Name the blood parasite species.
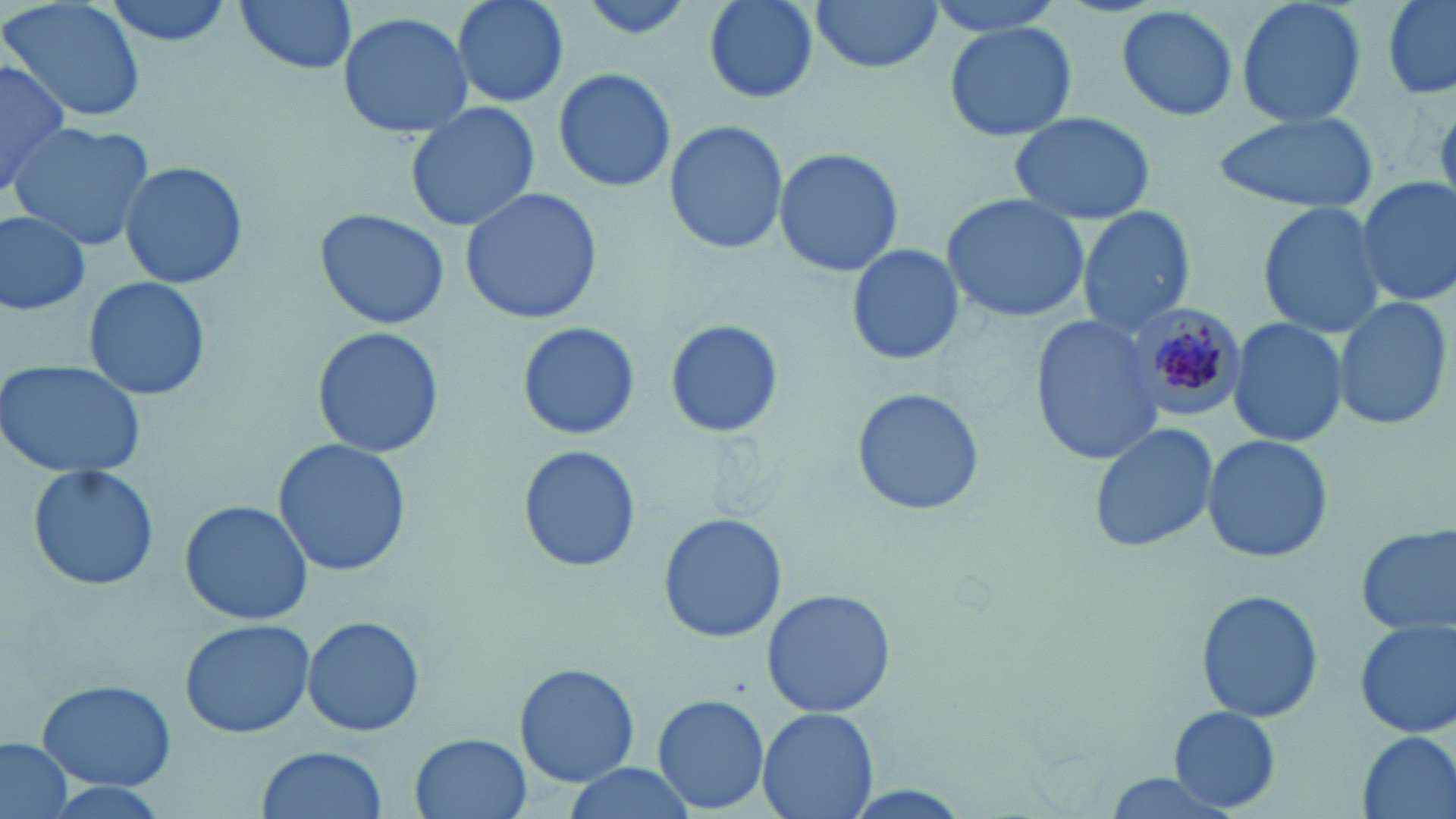

Plasmodium malariae.

Summary:
  - Coordinate format: approximate bounding boxes as named x1/y1/x2/y2 corners in pixels
  - Uninfected red blood cell locations: (x1=4, y1=0, x2=149, y2=123), (x1=101, y1=0, x2=233, y2=49), (x1=233, y1=0, x2=359, y2=77), (x1=448, y1=0, x2=569, y2=108), (x1=576, y1=0, x2=700, y2=41), (x1=700, y1=0, x2=821, y2=104), (x1=810, y1=0, x2=945, y2=74), (x1=924, y1=0, x2=1070, y2=41), (x1=1236, y1=0, x2=1366, y2=129), (x1=1380, y1=0, x2=1456, y2=98), (x1=1117, y1=4, x2=1238, y2=122), (x1=335, y1=11, x2=476, y2=139), (x1=944, y1=20, x2=1077, y2=143), (x1=0, y1=52, x2=69, y2=198), (x1=553, y1=65, x2=679, y2=194), (x1=406, y1=100, x2=540, y2=232), (x1=1007, y1=109, x2=1157, y2=224), (x1=1209, y1=112, x2=1377, y2=216), (x1=662, y1=121, x2=789, y2=254), (x1=8, y1=122, x2=155, y2=252), (x1=774, y1=147, x2=904, y2=279), (x1=117, y1=161, x2=247, y2=289), (x1=1351, y1=177, x2=1456, y2=308), (x1=459, y1=186, x2=603, y2=325), (x1=939, y1=194, x2=1091, y2=323), (x1=1255, y1=200, x2=1390, y2=339), (x1=1078, y1=205, x2=1196, y2=335), (x1=314, y1=207, x2=450, y2=330), (x1=0, y1=210, x2=93, y2=316), (x1=845, y1=243, x2=964, y2=367), (x1=80, y1=275, x2=216, y2=403), (x1=1331, y1=295, x2=1453, y2=433), (x1=1028, y1=313, x2=1166, y2=467), (x1=661, y1=320, x2=786, y2=440), (x1=1227, y1=320, x2=1349, y2=446), (x1=514, y1=323, x2=641, y2=442), (x1=311, y1=325, x2=445, y2=461), (x1=0, y1=358, x2=150, y2=480), (x1=849, y1=386, x2=986, y2=518), (x1=1088, y1=421, x2=1220, y2=554), (x1=1202, y1=432, x2=1333, y2=564), (x1=272, y1=438, x2=412, y2=579), (x1=516, y1=445, x2=643, y2=574), (x1=27, y1=463, x2=160, y2=593), (x1=178, y1=499, x2=314, y2=626), (x1=658, y1=513, x2=788, y2=643), (x1=1353, y1=524, x2=1456, y2=637), (x1=761, y1=587, x2=894, y2=719), (x1=1197, y1=589, x2=1324, y2=723), (x1=302, y1=615, x2=426, y2=738), (x1=178, y1=617, x2=318, y2=739), (x1=1354, y1=620, x2=1455, y2=740), (x1=515, y1=662, x2=638, y2=787), (x1=36, y1=679, x2=177, y2=791), (x1=652, y1=694, x2=771, y2=813), (x1=1168, y1=707, x2=1283, y2=812), (x1=757, y1=708, x2=878, y2=819), (x1=1355, y1=730, x2=1454, y2=819), (x1=411, y1=732, x2=533, y2=819), (x1=0, y1=735, x2=75, y2=819), (x1=257, y1=745, x2=388, y2=819), (x1=561, y1=761, x2=697, y2=817), (x1=1094, y1=770, x2=1246, y2=819)
  - Plasmodium malariae-infected red blood cell locations: (x1=1134, y1=309, x2=1248, y2=416)
  - Preparation: thin blood film
  - Stain: May-Grünwald-Giemsa
  - Image size: 1456×819 pixels
  - Field of view: single
  - Modality: light microscopy
  - Magnification: 1000x